Report the malaria status of this cell.
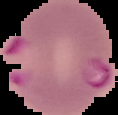

It is parasitized.

Summary:
  - Image type: segmented cell region on a black background
  - Image size: 118×115 pixels
  - Preparation: thin blood film